Comment on the morphology of the red blood cells.
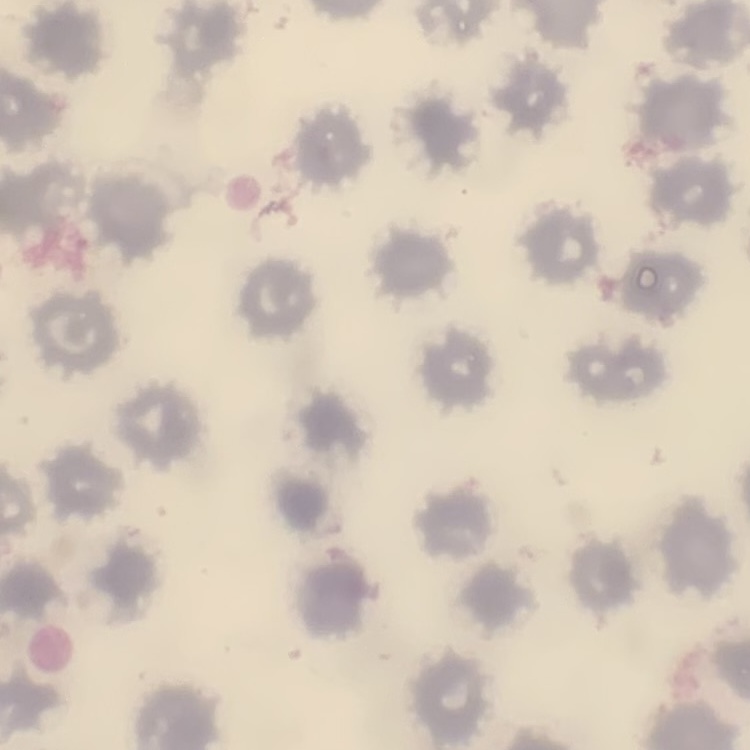
They show no rouleaux formation.

Field's or Giemsa stain. Thin blood smear. Square crop of a larger photomicrograph.